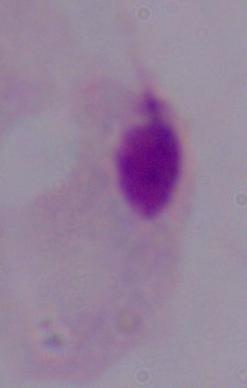 Photomicrograph. Captured at 1000x magnification. A trichomonad is seen.